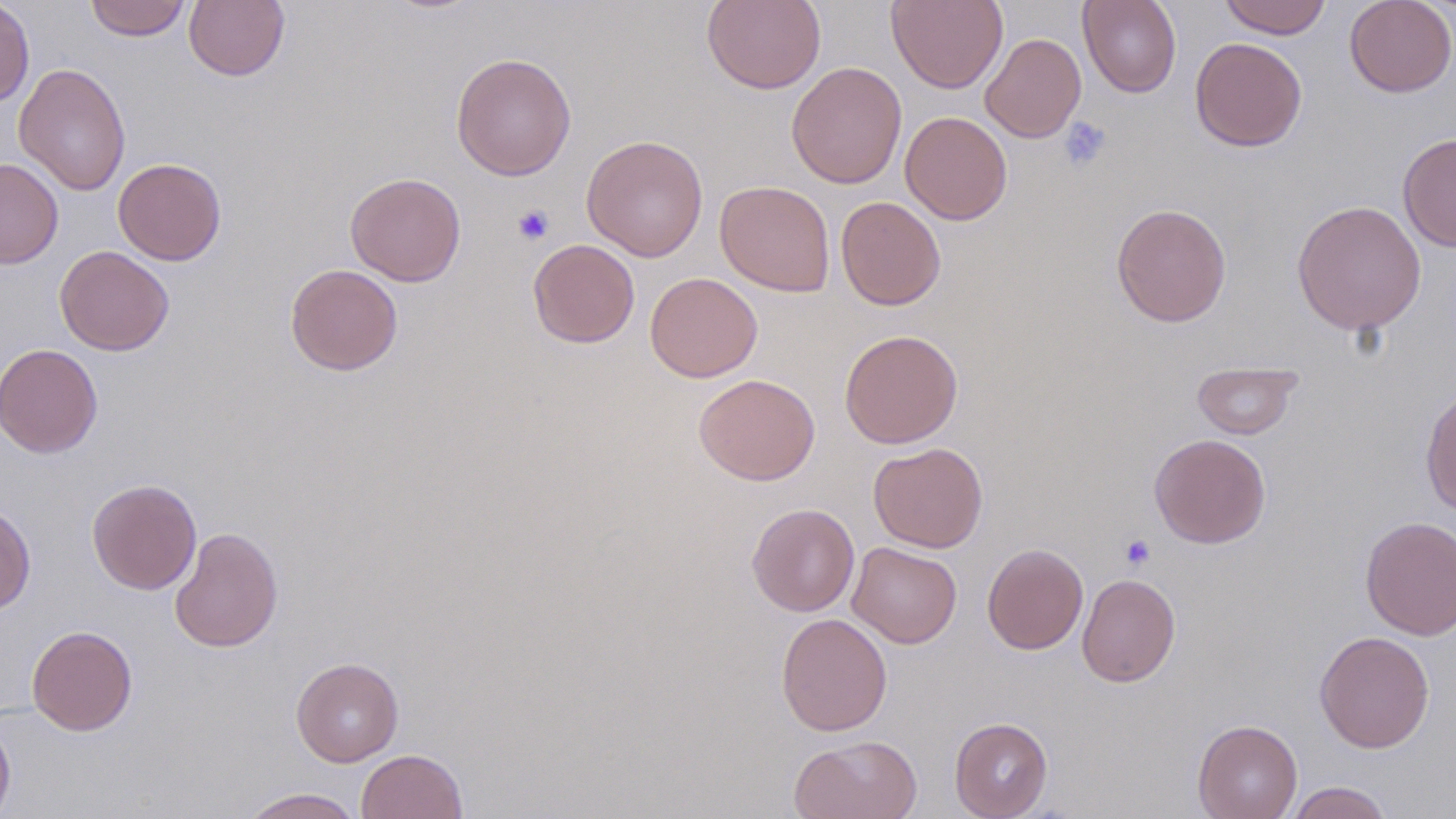
Approximate bounding boxes as (x1, y1, x2, y2) in pixels. Platelet locations: (1059, 116, 1112, 170), (512, 204, 555, 246), (1120, 533, 1155, 569). Uninfected red blood cell locations: (0, 0, 35, 108), (84, 0, 191, 41), (183, 0, 290, 82), (701, 0, 826, 94), (887, 0, 1008, 93), (1078, 0, 1181, 98), (1218, 0, 1332, 39), (1344, 0, 1456, 97), (980, 33, 1086, 143), (1190, 37, 1307, 152), (450, 52, 576, 181), (786, 62, 907, 189), (13, 63, 131, 196), (899, 111, 1013, 225), (1398, 131, 1456, 253), (581, 135, 709, 262), (0, 158, 63, 268), (113, 158, 227, 266), (345, 172, 466, 287), (715, 180, 835, 297), (835, 196, 946, 310), (1291, 199, 1427, 335), (1111, 203, 1232, 327), (527, 239, 640, 348), (54, 245, 174, 355), (285, 264, 403, 376), (644, 272, 763, 383), (839, 329, 963, 448), (0, 342, 103, 459), (1192, 361, 1301, 440), (693, 373, 820, 485), (1420, 385, 1456, 515), (1149, 433, 1272, 549), (868, 442, 988, 553), (87, 478, 202, 594), (0, 503, 36, 615), (746, 503, 859, 617), (1360, 515, 1456, 640), (169, 526, 284, 653), (847, 542, 962, 648), (982, 543, 1088, 654), (1077, 573, 1181, 687), (776, 613, 892, 736), (26, 625, 138, 735), (1314, 631, 1435, 753), (291, 657, 403, 766), (0, 715, 16, 819), (949, 717, 1053, 819), (1192, 719, 1303, 819), (788, 734, 923, 819), (357, 749, 467, 819), (1285, 781, 1394, 818), (239, 787, 364, 819). Slide-level diagnosis: negative for blood parasites. Thin blood smear. May-Grünwald-Giemsa-stained preparation. Captured at 1000x magnification. Image is 1456×819 pixels. One field of a larger specimen. Light microscopy.